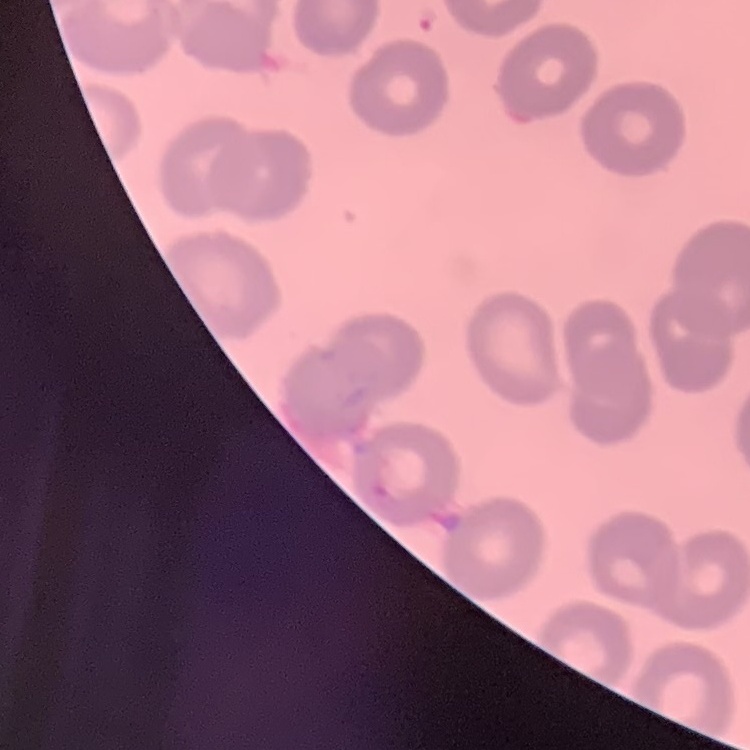
Summary:
  - Erythrocyte morphology: no rouleaux formation
  - Stain: Field's or Giemsa
  - Preparation: thin peripheral smear
  - Image type: one tile cut from a larger photomicrograph